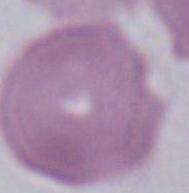

1000x magnification. An erythrocyte is shown. Micrograph.